Identify the cell.
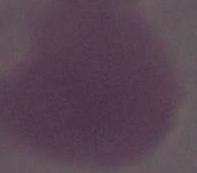
This is an erythrocyte.

Photomicrograph. 1000x magnification.